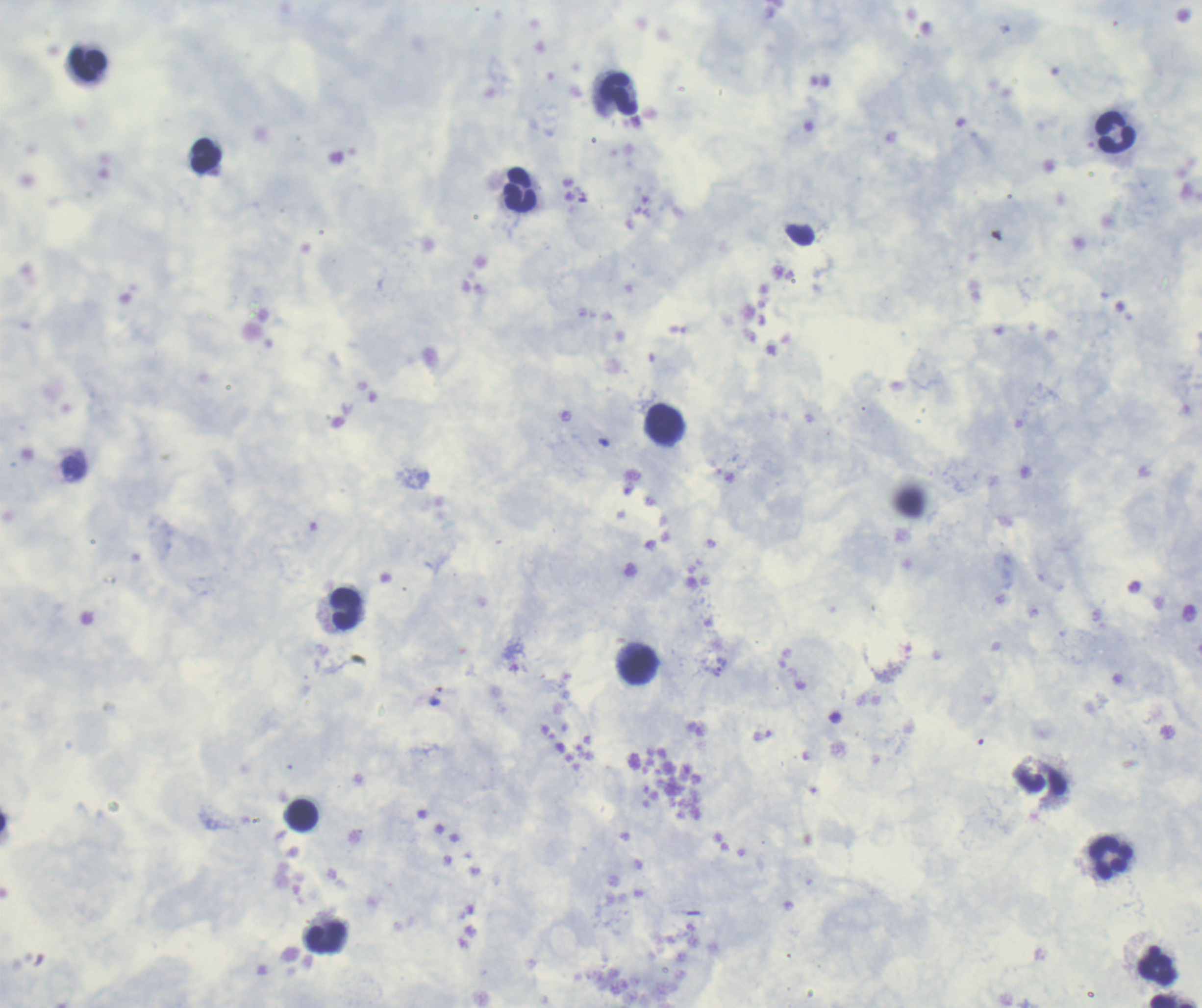

Approximate centers as (x, y) in pixels. Leukocyte locations: (88, 64), (620, 95), (1115, 132), (206, 157), (520, 190), (665, 425), (346, 608), (638, 666), (1043, 783), (303, 814), (1112, 858), (327, 939), (1157, 966), (1173, 1001). Thick blood smear. Previously used in an actual diagnosis. 100x magnification. Result: negative for Plasmodium parasites. Romanowsky stain. Coloration quality: good. Background quality: satisfactory. Single field of view. Image is 1202×1008 pixels.